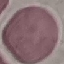
Result: negative for malaria parasites. Acquired by smartphone through the microscope eyepiece. Cell patch, automatically extracted from a larger field of view and resized to 64 × 64 pixels. Thin smear of blood. Giemsa stain.